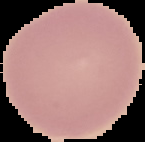
Summary:
  - Preparation: thin blood smear
  - Image type: segmented cell region on a black background
  - Image size: 145×142 pixels
  - Malaria status: uninfected